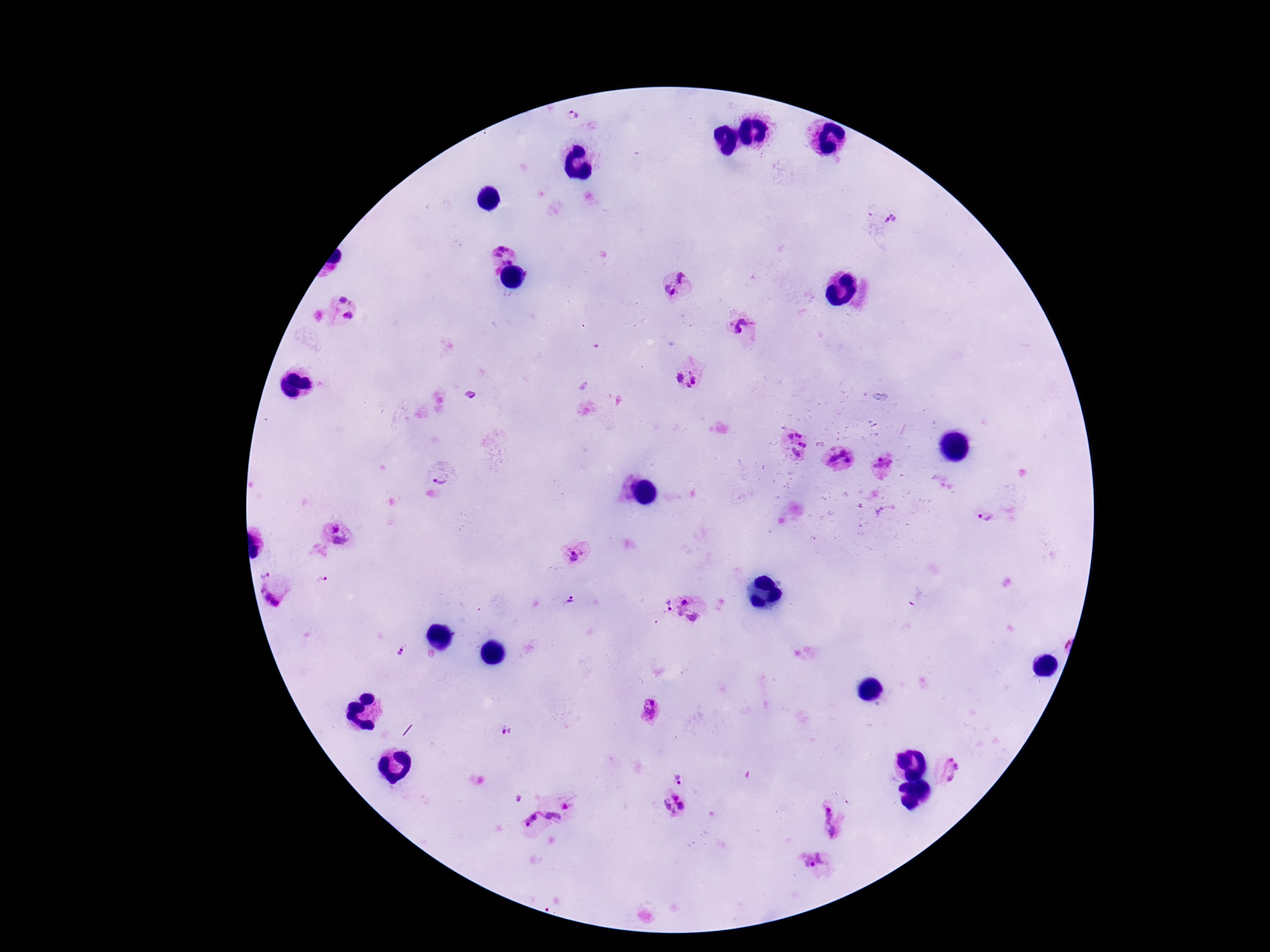

Approximate centers as [x, y] in pixels.
Summary:
  - Plasmodium parasite locations: [572, 115], [892, 222], [505, 254], [684, 277], [670, 290], [346, 298], [349, 317], [740, 327], [688, 378], [795, 443], [840, 461], [887, 465], [440, 475], [984, 517], [335, 527], [339, 542], [578, 554], [264, 571], [323, 578], [273, 593], [570, 599], [684, 602], [668, 604], [691, 615], [399, 652], [649, 713], [507, 731], [948, 771], [678, 775], [519, 799], [566, 806], [672, 807], [552, 817], [532, 820], [827, 821], [813, 863]
  - Patient malaria status: infected
  - Stain: Giemsa
  - Preparation: thick peripheral-blood smear
  - Capture: smartphone camera through the microscope eyepiece
  - Image size: 1270×952 pixels
  - Field of view: one from this slide
  - Magnification: 100x